Outline each blood parasite and name the species.
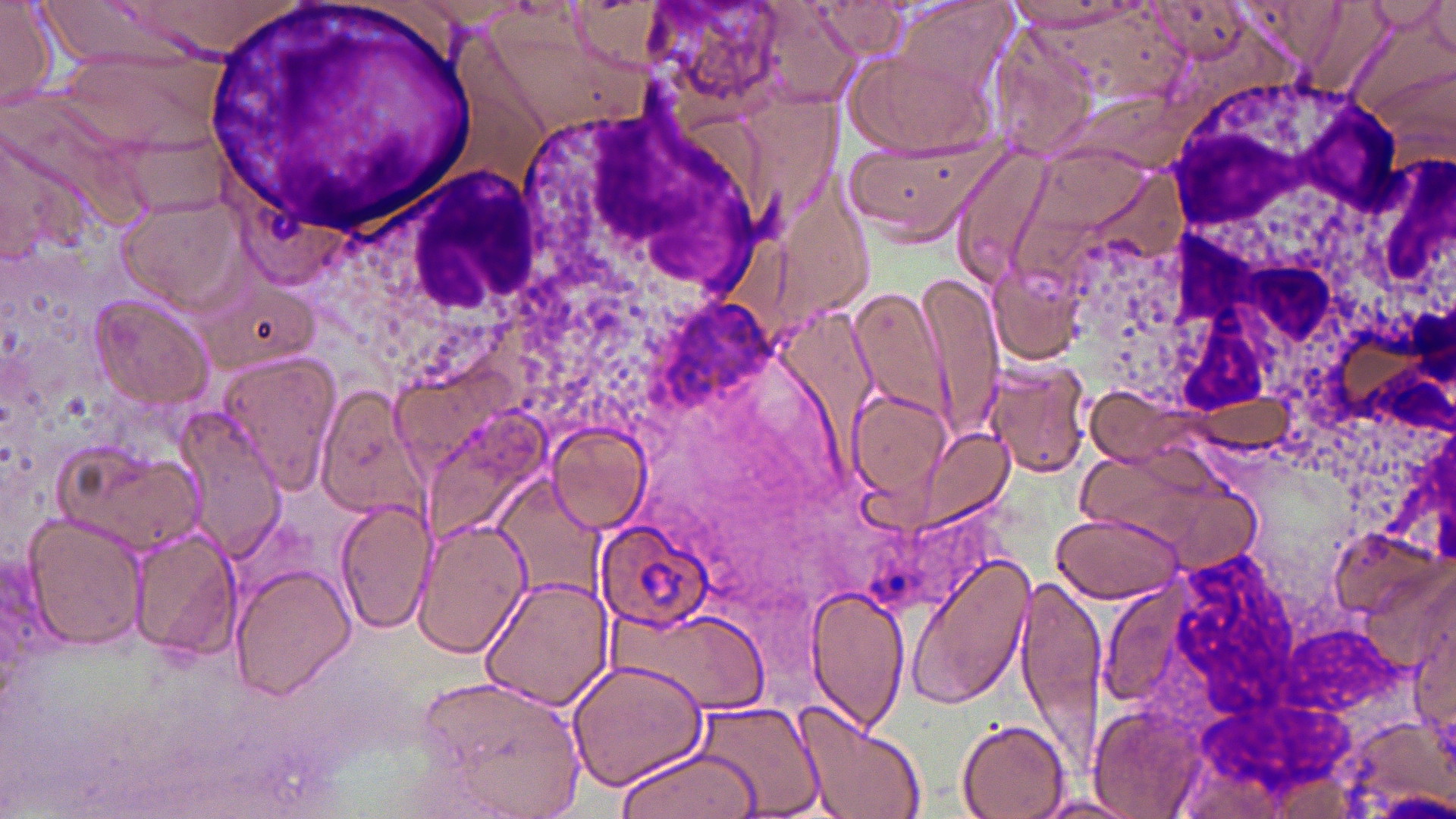
Approximate bounding boxes as named x1/y1/x2/y2 corners in pixels.
Plasmodium ovale-infected red blood cells: (x1=593, y1=518, x2=715, y2=633).
No Plasmodium falciparum, Plasmodium malariae, Plasmodium vivax, Babesia divergens, or Trypanosoma brucei observed.

Uninfected red blood cell locations: (x1=108, y1=0, x2=321, y2=59), (x1=638, y1=0, x2=795, y2=122), (x1=1235, y1=0, x2=1351, y2=72), (x1=0, y1=1, x2=55, y2=112), (x1=806, y1=1, x2=911, y2=62), (x1=1146, y1=1, x2=1258, y2=68), (x1=1430, y1=1, x2=1456, y2=61), (x1=32, y1=3, x2=167, y2=63), (x1=1334, y1=4, x2=1453, y2=133), (x1=477, y1=20, x2=652, y2=142), (x1=51, y1=37, x2=240, y2=165), (x1=847, y1=45, x2=997, y2=162), (x1=835, y1=125, x2=1006, y2=242), (x1=0, y1=127, x2=96, y2=268), (x1=949, y1=142, x2=1054, y2=285), (x1=115, y1=194, x2=254, y2=311), (x1=913, y1=271, x2=1006, y2=438), (x1=199, y1=278, x2=322, y2=375), (x1=849, y1=286, x2=951, y2=421), (x1=88, y1=295, x2=217, y2=409), (x1=216, y1=353, x2=342, y2=492), (x1=984, y1=358, x2=1095, y2=480), (x1=315, y1=386, x2=426, y2=520), (x1=845, y1=386, x2=955, y2=506), (x1=422, y1=408, x2=551, y2=540), (x1=546, y1=423, x2=650, y2=533), (x1=915, y1=427, x2=1013, y2=528), (x1=57, y1=440, x2=208, y2=559), (x1=1079, y1=445, x2=1231, y2=548), (x1=497, y1=474, x2=608, y2=601), (x1=335, y1=496, x2=437, y2=637), (x1=1052, y1=510, x2=1182, y2=604), (x1=22, y1=513, x2=150, y2=652), (x1=411, y1=517, x2=530, y2=658), (x1=130, y1=526, x2=243, y2=662), (x1=1330, y1=526, x2=1445, y2=630), (x1=903, y1=553, x2=1036, y2=712), (x1=229, y1=562, x2=357, y2=701), (x1=1015, y1=565, x2=1107, y2=763), (x1=480, y1=574, x2=614, y2=709), (x1=1403, y1=579, x2=1456, y2=733), (x1=805, y1=584, x2=910, y2=734), (x1=604, y1=608, x2=766, y2=711), (x1=571, y1=658, x2=708, y2=792), (x1=415, y1=675, x2=586, y2=814), (x1=694, y1=699, x2=824, y2=819), (x1=793, y1=701, x2=930, y2=819), (x1=1084, y1=707, x2=1209, y2=814), (x1=1334, y1=714, x2=1453, y2=816), (x1=957, y1=719, x2=1072, y2=818), (x1=609, y1=744, x2=762, y2=817), (x1=1031, y1=794, x2=1145, y2=817). White blood cell locations: (x1=202, y1=1, x2=486, y2=238), (x1=1160, y1=75, x2=1454, y2=408), (x1=517, y1=106, x2=783, y2=341). Slide-level diagnosis: Plasmodium ovale. One field of a larger specimen. Optical microscopy. Image is 1456×819 pixels. 1000x magnification. Thin blood smear. May-Grünwald-Giemsa-stained preparation.